Report the malaria status of this cell.
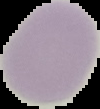

Uninfected.

{
  "image_type": "segmented cell region with the area outside set to black",
  "preparation": "thin blood smear",
  "image_size": "100×109 pixels"
}